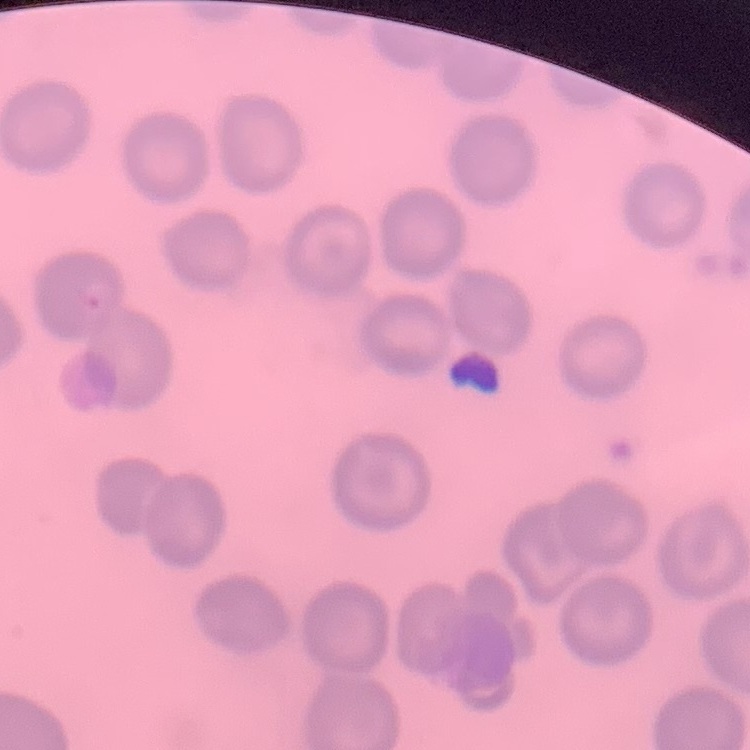
Summary:
  - Red blood cell morphology: no rouleaux formation
  - Preparation: thin blood film
  - Stain: Field's or Giemsa
  - Image type: square crop of a larger photomicrograph